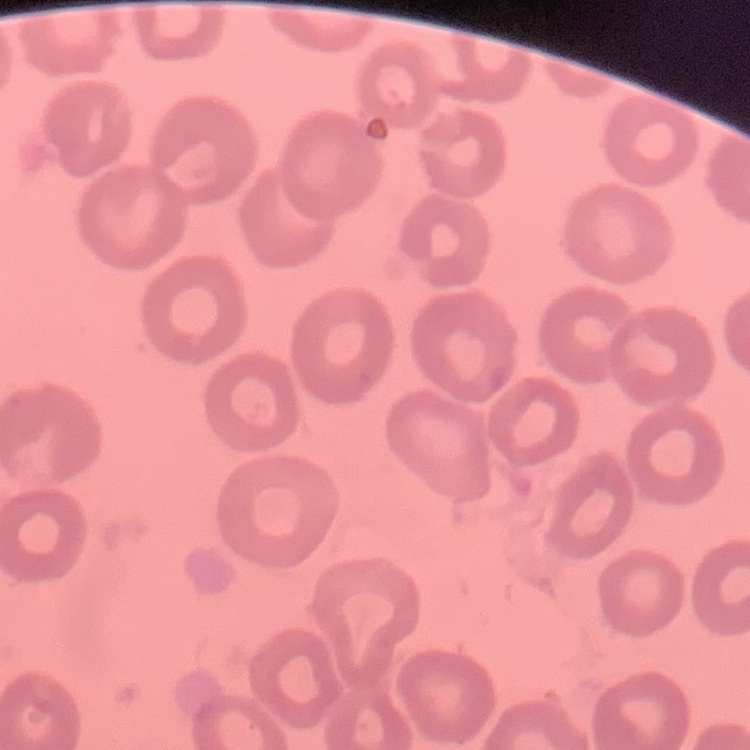 The red blood cells show no rouleaux formation. Stained with either Field's or Giemsa. Thin blood smear. One tile cut from a larger photomicrograph.